Assess the morphology of the red blood cells.
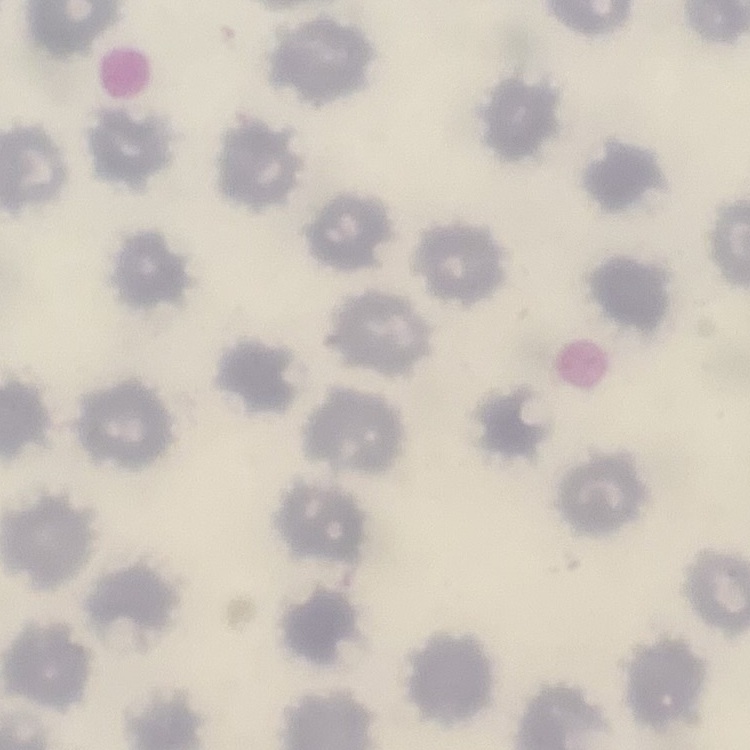
They show no rouleaux formation.

stain = Field's or Giemsa
image type = one tile cut from a larger photomicrograph
preparation = thin blood smear